State the blood parasite species.
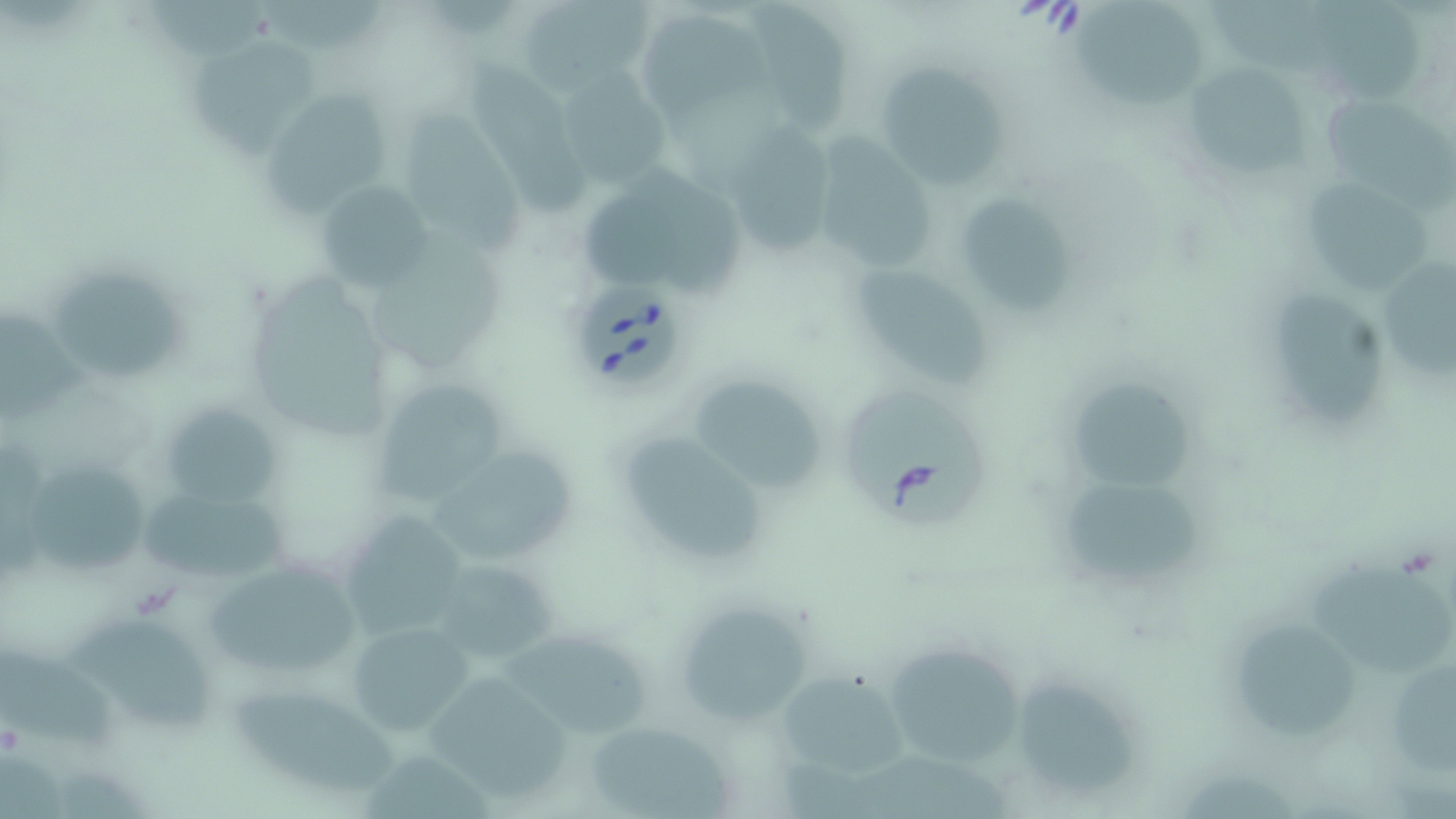

Babesia divergens.

preparation: thin blood film
magnification: 1000x
babesia_divergens_infected_red_blood_cell_locations: 'approximate bounding boxes as [x1, y1, x2, y2] in pixels: [574, 279, 687, 389], [841, 389, 988, 526]'
modality: optical microscopy
image_size: 1456×819 pixels
stain: May-Grünwald-Giemsa
field_of_view: single
uninfected_red_blood_cell_locations: 'approximate bounding boxes as [x1, y1, x2, y2] in pixels: [146, 0, 272, 61], [747, 0, 852, 133], [1075, 0, 1201, 106], [1311, 0, 1426, 100], [524, 1, 658, 95], [638, 17, 769, 121], [182, 38, 319, 154], [868, 55, 1011, 188], [470, 63, 592, 219], [556, 66, 671, 194], [1188, 67, 1310, 174], [266, 89, 393, 214], [1319, 90, 1450, 204], [402, 103, 526, 255], [733, 121, 837, 257], [806, 131, 939, 270], [574, 169, 747, 299], [1301, 174, 1432, 291], [315, 176, 437, 293], [953, 193, 1072, 314], [1379, 255, 1456, 379], [850, 262, 991, 387], [53, 267, 186, 377], [1275, 290, 1386, 422], [1, 306, 88, 418], [367, 373, 517, 512], [1067, 376, 1203, 490], [699, 377, 826, 498], [160, 400, 280, 508], [619, 424, 767, 562], [436, 441, 575, 559], [24, 457, 145, 575], [137, 471, 288, 593], [1067, 476, 1205, 588], [334, 506, 475, 642], [426, 556, 564, 672], [203, 559, 361, 678], [1308, 566, 1452, 676], [680, 607, 813, 731], [68, 612, 214, 733], [347, 619, 476, 737], [1240, 622, 1357, 735], [496, 630, 648, 737], [880, 639, 1029, 771], [2, 641, 123, 749], [1391, 659, 1456, 782], [424, 667, 576, 795], [774, 669, 911, 782], [1017, 682, 1142, 795], [232, 689, 405, 793], [583, 718, 737, 819], [358, 749, 496, 819], [1179, 771, 1297, 817]'